Classify this cell by malaria status.
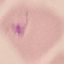
Parasitized.

Thin smear of blood. Giemsa stain. Cell patch, automatically extracted from a larger field of view and resized to 64 × 64 pixels. Acquired by smartphone through the microscope eyepiece.